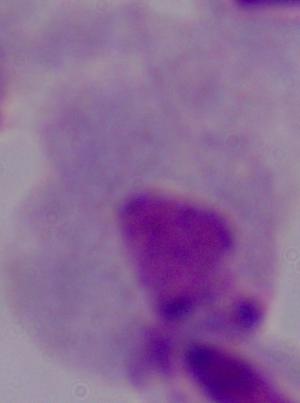
Summary:
  - Magnification: 1000x
  - Modality: micrograph
  - Identification: trichomonad